Report the malaria status of this cell.
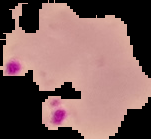

Parasitized.

image_size: 151×139 pixels
preparation: thin blood smear
image_type: segmented cell region on a black background